Identify the blood parasite species.
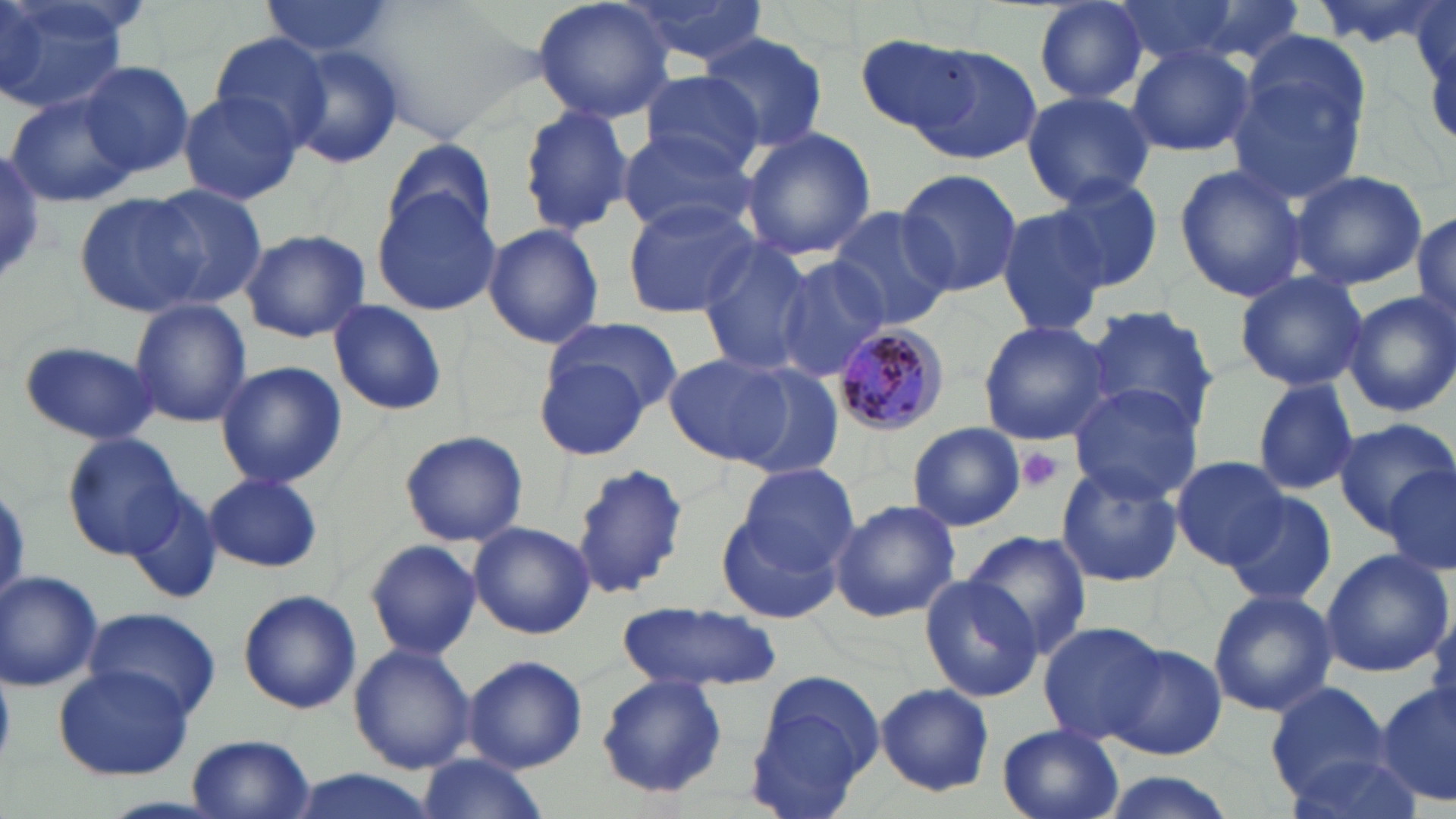

Plasmodium malariae.

modality = light microscopy
preparation = thin blood smear
stain = May-Grünwald-Giemsa
platelet locations = approximate bounding boxes as (x1, y1, x2, y2) in pixels: (1015, 446, 1066, 493)
magnification = 1000x
field of view = one of a larger specimen
Plasmodium malariae-infected red blood cell locations = approximate bounding boxes as (x1, y1, x2, y2) in pixels: (831, 324, 949, 438)
image size = 1456×819 pixels
uninfected red blood cell locations = approximate bounding boxes as (x1, y1, x2, y2) in pixels: (0, 0, 128, 113), (256, 0, 401, 59), (532, 0, 673, 123), (616, 0, 773, 70), (1113, 0, 1245, 67), (1308, 0, 1446, 50), (1029, 1, 1150, 106), (696, 32, 831, 150), (857, 33, 986, 140), (206, 34, 334, 145), (1227, 36, 1372, 202), (283, 41, 406, 171), (1126, 43, 1255, 157), (908, 45, 1040, 164), (79, 62, 194, 178), (636, 71, 766, 175), (1018, 89, 1156, 209), (5, 90, 136, 209), (178, 90, 304, 205), (517, 105, 632, 236), (741, 126, 877, 260), (617, 128, 756, 235), (382, 139, 496, 242), (0, 152, 48, 283), (1174, 163, 1307, 303), (895, 168, 1023, 299), (1288, 169, 1428, 289), (1048, 177, 1165, 293), (140, 184, 267, 309), (75, 192, 203, 316), (372, 192, 501, 315), (620, 197, 760, 317), (825, 206, 954, 332), (993, 207, 1108, 337), (1412, 214, 1456, 330), (482, 222, 605, 349), (239, 228, 370, 343), (694, 241, 814, 375), (772, 257, 887, 383), (1233, 270, 1369, 391), (1345, 290, 1456, 417), (129, 300, 253, 428), (329, 300, 447, 416), (1085, 304, 1220, 433), (545, 315, 683, 412), (977, 319, 1113, 445), (19, 340, 164, 446), (664, 351, 797, 466), (536, 355, 652, 460), (216, 361, 346, 488), (732, 363, 847, 479), (1250, 378, 1359, 496), (1065, 385, 1205, 505), (1333, 418, 1455, 536), (908, 422, 1025, 531), (400, 429, 528, 547), (61, 432, 187, 558), (1171, 455, 1287, 569), (571, 461, 692, 600), (736, 462, 859, 570), (1383, 463, 1456, 578), (1055, 464, 1182, 588), (203, 472, 324, 573), (126, 491, 224, 607), (1222, 491, 1337, 606), (828, 498, 961, 622), (719, 509, 840, 623), (469, 521, 595, 639), (961, 530, 1094, 658), (365, 539, 481, 660), (1319, 548, 1453, 677), (0, 570, 102, 691), (921, 572, 1042, 702), (1207, 587, 1337, 718), (237, 589, 361, 715), (619, 601, 781, 694), (81, 607, 222, 721), (1427, 613, 1456, 729), (1037, 623, 1168, 747), (349, 644, 477, 773), (1108, 645, 1228, 762), (463, 654, 587, 771), (54, 665, 193, 780), (744, 667, 883, 817), (595, 674, 728, 798), (876, 682, 994, 797), (1267, 682, 1391, 795), (1376, 686, 1455, 808), (997, 725, 1124, 819), (188, 734, 316, 818), (1280, 750, 1425, 819), (416, 754, 547, 819), (284, 769, 436, 819), (1093, 773, 1238, 819)